Point out each leukocyte.
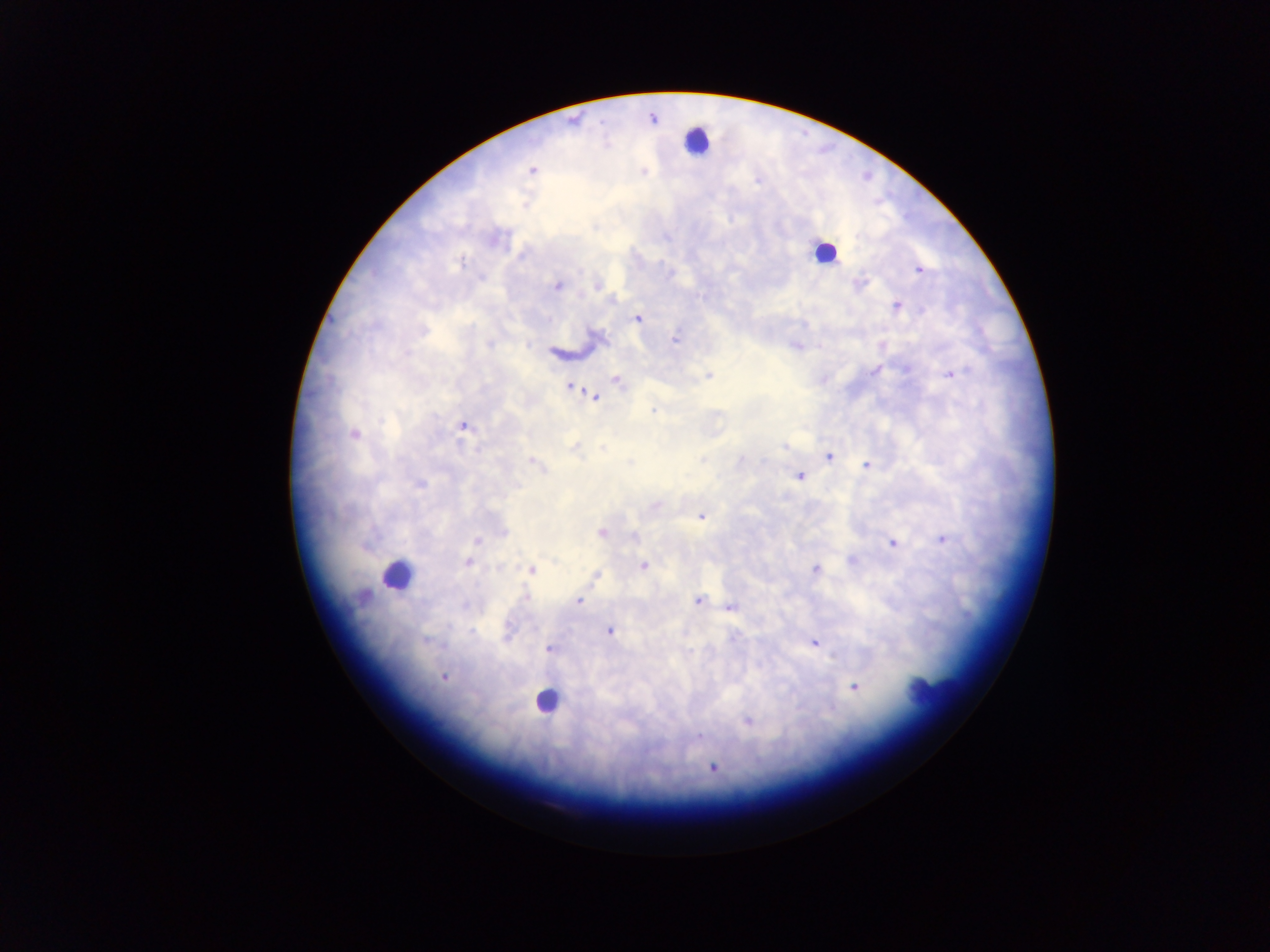

Approximate centers as {x, y} in pixels.
Leukocytes: {697, 141}, {823, 252}, {396, 574}, {931, 687}, {546, 700}.

country: Ghana
capture: mobile-phone photograph through a microscope
malaria_parasite_locations: 'approximate centers as {x, y} in pixels: {652, 118}, {532, 171}, {757, 180}, {919, 270}, {860, 284}, {597, 285}, {557, 286}, {612, 299}, {897, 306}, {550, 319}, {637, 319}, {424, 331}, {675, 340}, {488, 344}, {874, 371}, {950, 374}, {709, 375}, {617, 380}, {571, 387}, {594, 397}, {653, 412}, {716, 415}, {464, 426}, {354, 434}, {784, 445}, {574, 446}, {603, 448}, {829, 456}, {701, 460}, {741, 460}, {533, 461}, {867, 465}, {799, 476}, {419, 483}, {655, 506}, {701, 516}, {503, 532}, {601, 532}, {633, 536}, {943, 540}, {476, 541}, {893, 543}, {852, 560}, {468, 562}, {644, 565}, {499, 568}, {815, 569}, {531, 570}, {596, 575}, {526, 596}, {697, 600}, {579, 601}, {731, 606}, {610, 631}, {735, 636}, {425, 640}, {815, 643}, {549, 649}, {444, 676}, {854, 687}, {748, 721}, {699, 736}, {713, 768}'
field_of_view: single
image_size: 1270×952 pixels
preparation: thick blood smear